Locate every Plasmodium parasite.
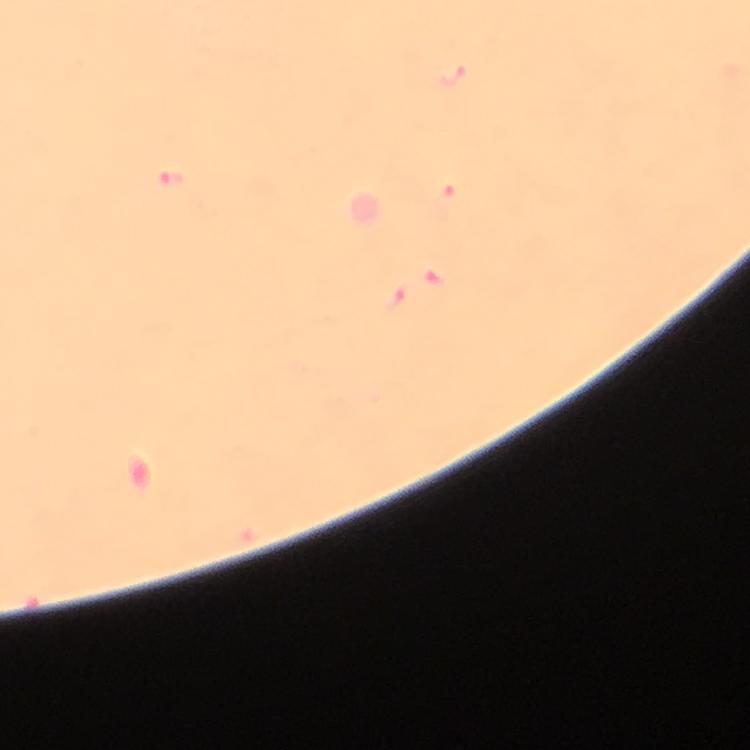
Approximate object centers, in pixels from the top-left corner.
Plasmodium parasites: (x=452, y=73), (x=169, y=180), (x=448, y=194), (x=435, y=279), (x=395, y=298).

{
  "preparation": "thick smear",
  "immersion_oil": "used",
  "stain": "Giemsa",
  "capture": "smartphone mounted on the microscope",
  "image_size": "750×750 pixels",
  "cropped_from": "a single field of view",
  "magnification": "100x",
  "context": "from a diagnostic examination for malaria"
}